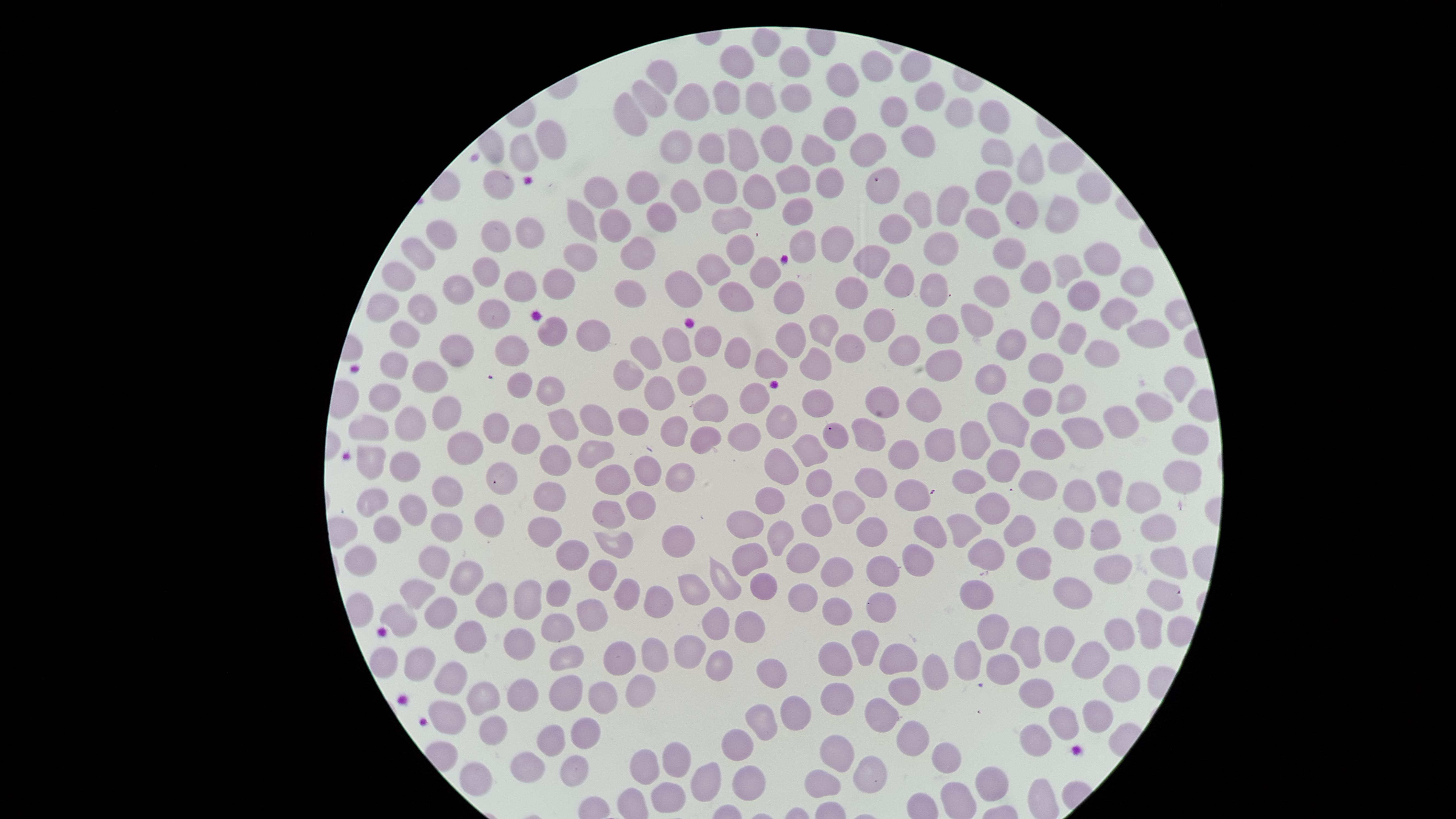

Approximate marker points as {x, y} in pixels.
Summary:
  - Uninfected red blood cells: {797, 57}, {743, 60}, {910, 69}, {873, 71}, {666, 75}, {848, 81}, {731, 92}, {792, 96}, {655, 98}, {929, 98}, {761, 100}, {697, 103}, {635, 111}, {955, 111}, {895, 114}, {992, 119}, {840, 122}, {547, 133}, {773, 139}, {742, 140}, {916, 140}, {517, 146}, {673, 146}, {867, 146}, {819, 149}, {713, 151}, {996, 158}, {1030, 167}, {501, 177}, {792, 177}, {724, 179}, {823, 182}, {644, 184}, {992, 184}, {761, 186}, {881, 186}, {1094, 187}, {602, 190}, {688, 194}, {948, 200}, {1022, 207}, {919, 210}, {662, 212}, {1063, 212}, {797, 216}, {584, 219}, {732, 219}, {614, 223}, {892, 227}, {983, 227}, {528, 230}, {445, 236}, {496, 236}, {836, 244}, {804, 246}, {946, 246}, {636, 247}, {740, 248}, {1010, 249}, {1101, 251}, {424, 253}, {582, 254}, {870, 258}, {713, 260}, {1071, 266}, {487, 267}, {766, 272}, {407, 274}, {1029, 277}, {522, 278}, {894, 278}, {560, 284}, {1138, 285}, {933, 286}, {993, 288}, {687, 289}, {458, 290}, {628, 290}, {853, 293}, {1083, 295}, {737, 296}, {790, 300}, {1121, 307}, {425, 309}, {388, 310}, {494, 311}, {974, 319}, {1043, 319}, {880, 323}, {827, 326}, {940, 328}, {553, 331}, {595, 331}, {707, 331}, {1146, 331}, {791, 332}, {408, 336}, {1072, 336}, {675, 343}, {1009, 345}, {645, 348}, {903, 348}, {455, 349}, {730, 349}, {850, 349}, {516, 350}, {1094, 353}, {771, 361}, {815, 363}, {946, 365}, {1050, 367}, {397, 369}, {632, 369}, {431, 372}, {692, 376}, {994, 379}, {1177, 380}, {522, 382}, {551, 385}, {656, 389}, {755, 392}, {1067, 395}, {383, 397}, {886, 398}, {1042, 401}, {815, 403}, {930, 403}, {444, 406}, {713, 407}, {1157, 409}, {593, 415}, {1015, 416}, {631, 419}, {1121, 419}, {410, 420}, {564, 421}, {492, 422}, {780, 423}, {679, 424}, {378, 427}, {1080, 427}, {749, 432}, {971, 432}, {869, 433}, {529, 434}, {707, 435}, {839, 436}, {1195, 437}, {1045, 442}, {936, 443}, {464, 445}, {596, 450}, {813, 450}, {905, 450}, {553, 455}, {999, 460}, {371, 463}, {403, 464}, {785, 465}, {649, 468}, {1179, 474}, {612, 477}, {683, 477}, {969, 478}, {496, 480}, {872, 480}, {1036, 480}, {822, 481}, {443, 486}, {1109, 486}, {916, 492}, {1071, 492}, {1140, 494}, {777, 495}, {373, 496}, {551, 498}, {852, 498}, {409, 501}, {640, 502}, {996, 505}, {610, 509}, {489, 517}, {818, 520}, {445, 521}, {869, 524}, {385, 526}, {1159, 527}, {748, 528}, {1072, 530}, {1017, 531}, {967, 532}, {928, 534}, {543, 535}, {1107, 535}, {784, 536}, {679, 540}, {615, 543}, {565, 553}, {991, 553}, {361, 557}, {796, 557}, {752, 558}, {916, 560}, {1036, 562}, {1170, 562}, {435, 565}, {1109, 565}, {886, 568}, {839, 570}, {606, 574}, {464, 582}, {728, 584}, {761, 587}, {554, 591}, {976, 591}, {1075, 591}, {798, 593}, {419, 594}, {694, 594}, {628, 596}, {1163, 597}, {526, 598}, {359, 603}, {497, 603}, {657, 603}, {839, 610}, {876, 610}, {441, 611}, {400, 617}, {594, 617}, {748, 624}, {1150, 624}, {718, 626}, {560, 629}, {1123, 636}, {469, 639}, {1028, 642}, {520, 643}, {1054, 646}, {690, 648}, {863, 651}, {655, 656}, {834, 656}, {967, 656}, {716, 658}, {901, 658}, {620, 659}, {1094, 659}, {572, 660}, {424, 662}, {385, 664}, {936, 666}, {1009, 668}, {767, 671}, {449, 676}, {634, 681}, {1124, 684}, {838, 689}, {907, 692}, {568, 693}, {604, 693}, {525, 695}, {1037, 695}, {491, 699}, {794, 708}, {762, 712}, {1097, 712}, {883, 714}, {455, 717}, {1062, 719}, {498, 727}, {919, 731}, {588, 734}, {740, 742}, {557, 743}, {1042, 743}, {833, 753}, {948, 753}, {642, 761}, {678, 763}, {530, 767}, {576, 770}, {868, 778}, {475, 781}, {710, 781}, {749, 781}, {997, 782}, {821, 784}, {667, 793}
  - Stain: Giemsa
  - Visible region: circular
  - Preparation: thin blood film
  - Capture: smartphone photograph through the microscope eyepiece
  - Presence: no malaria parasites detected
  - Field of view: single
  - Image size: 1456×819 pixels